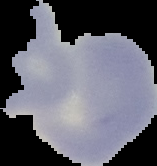
Summary:
  - Preparation: thin blood film
  - Image type: cell region segmented out of the field of view; surrounding area masked to black
  - Result: no Plasmodium parasites seen
  - Image size: 157×166 pixels